State the blood parasite species.
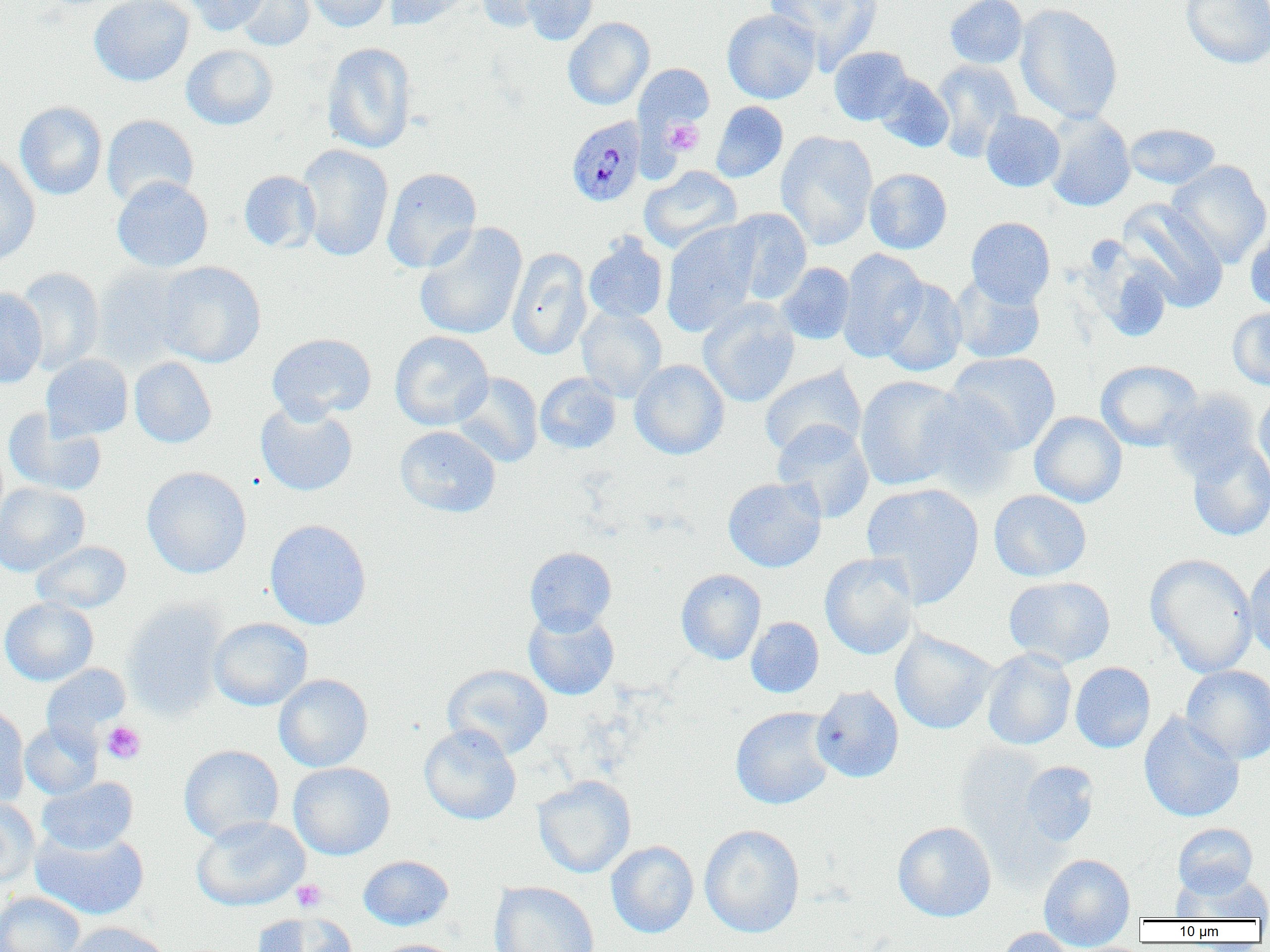
Plasmodium malariae.

Summary:
  - Coordinate format: approximate bounding boxes as (x1, y1, x2, y2) in pixels
  - Uninfected red blood cell locations: (89, 0, 194, 86), (183, 0, 269, 35), (230, 0, 315, 51), (303, 0, 392, 32), (387, 0, 473, 30), (473, 0, 557, 32), (520, 0, 599, 45), (765, 0, 883, 69), (944, 0, 1028, 69), (1181, 0, 1269, 69), (1015, 4, 1123, 124), (722, 9, 821, 104), (563, 17, 655, 110), (321, 42, 417, 154), (181, 44, 278, 130), (829, 46, 914, 125), (931, 60, 1022, 161), (634, 63, 714, 133), (873, 74, 954, 152), (15, 101, 107, 200), (711, 101, 788, 182), (981, 111, 1065, 192), (1043, 112, 1135, 212), (101, 114, 199, 208), (1124, 123, 1220, 189), (775, 131, 878, 250), (297, 144, 394, 262), (0, 152, 41, 268), (1166, 160, 1270, 267), (639, 166, 742, 253), (381, 167, 482, 273), (864, 168, 952, 254), (239, 170, 321, 253), (112, 176, 213, 273), (1117, 199, 1230, 311), (724, 208, 812, 304), (966, 217, 1055, 307), (661, 221, 761, 335), (413, 222, 527, 340), (1245, 226, 1270, 313), (583, 234, 668, 324), (507, 248, 592, 360), (836, 249, 929, 362), (154, 261, 266, 368), (776, 262, 856, 344), (91, 264, 193, 368), (14, 267, 105, 375), (950, 274, 1046, 364), (877, 277, 967, 377), (0, 288, 47, 388), (698, 299, 800, 408), (576, 306, 667, 401), (1228, 306, 1270, 390), (390, 331, 494, 431), (266, 333, 377, 423), (946, 352, 1061, 453), (41, 354, 133, 441), (129, 356, 217, 448), (630, 359, 729, 460), (1096, 360, 1203, 451), (759, 366, 866, 460), (452, 372, 543, 467), (535, 373, 621, 453), (854, 376, 968, 491), (912, 390, 1020, 496), (1163, 390, 1263, 484), (1254, 390, 1270, 489), (255, 401, 358, 497), (3, 409, 107, 497), (1030, 411, 1127, 507), (772, 420, 874, 523), (394, 425, 501, 517), (1186, 442, 1270, 541), (141, 466, 252, 578), (723, 476, 827, 573), (0, 482, 89, 576), (861, 482, 985, 607), (989, 489, 1092, 582), (264, 519, 371, 629), (32, 541, 131, 613), (524, 547, 617, 634), (819, 552, 920, 660), (1146, 553, 1258, 677), (1244, 555, 1270, 660), (676, 569, 766, 665), (1003, 576, 1116, 669), (0, 597, 98, 686), (123, 600, 228, 719), (523, 609, 620, 700), (746, 617, 824, 698), (209, 618, 312, 711), (890, 629, 998, 734), (981, 648, 1077, 750), (1070, 662, 1156, 753), (41, 664, 131, 747), (442, 664, 552, 760), (1181, 665, 1270, 764), (274, 674, 373, 772), (811, 685, 904, 783), (0, 705, 30, 807), (731, 707, 837, 810), (1139, 712, 1245, 823), (19, 721, 102, 800), (419, 724, 521, 825), (179, 745, 284, 844), (1019, 761, 1099, 847), (289, 762, 395, 859), (532, 775, 636, 878), (37, 776, 138, 855), (0, 797, 41, 888), (191, 816, 310, 911), (893, 821, 996, 922), (1172, 822, 1258, 897), (699, 824, 805, 938), (31, 827, 150, 920), (606, 841, 699, 938), (1038, 853, 1136, 950), (358, 855, 454, 930), (1172, 871, 1270, 921), (489, 881, 600, 952), (0, 892, 85, 952), (251, 912, 358, 952), (64, 921, 170, 952), (993, 927, 1081, 952), (373, 939, 465, 952)
  - Platelet locations: (663, 119, 704, 155), (101, 721, 146, 764), (291, 879, 327, 912)
  - Plasmodium malariae-infected red blood cell locations: (565, 116, 646, 207)
  - Image size: 1270×952 pixels
  - Preparation: thin blood film
  - Field of view: single
  - Magnification: 1000x
  - Modality: optical microscopy